Comment on the morphology of the erythrocytes.
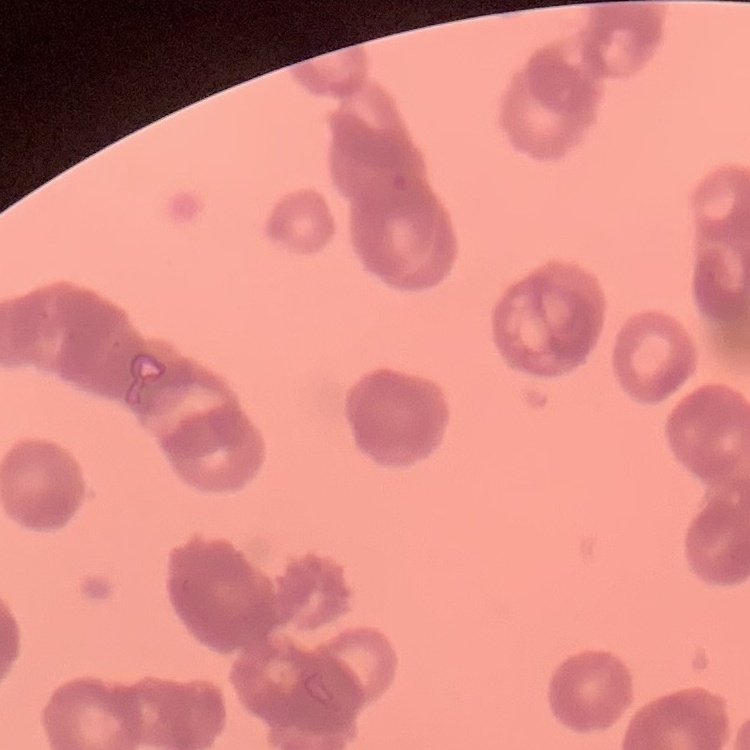
Rouleaux formation.

image type = one tile cut from a larger photomicrograph
stain = Field's or Giemsa
preparation = thin peripheral smear